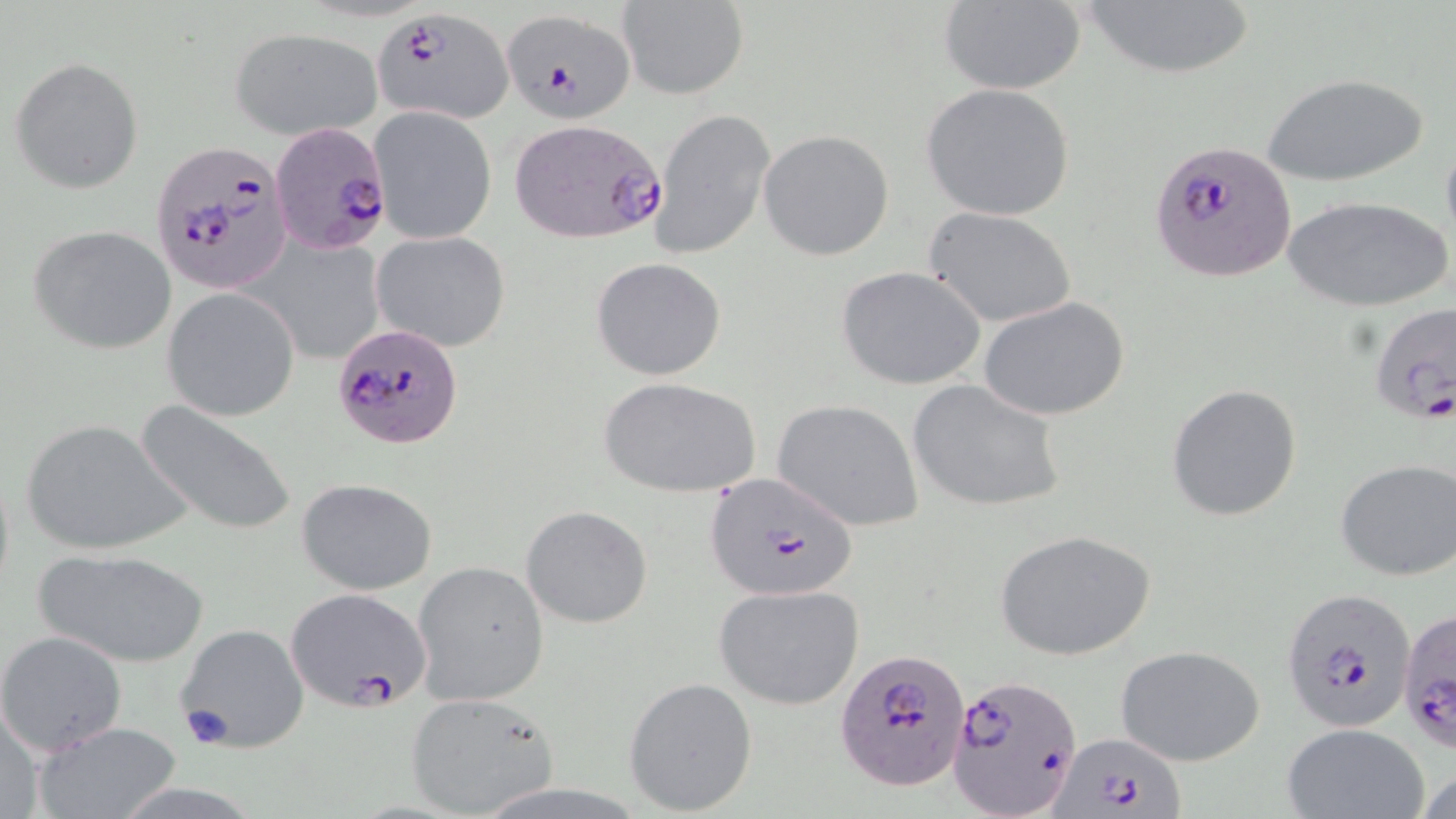

Summary:
  - Coordinate format: approximate bounding boxes as (x1, y1, x2, y2) in pixels
  - Plasmodium falciparum-infected red blood cell locations (subset): (373, 7, 514, 124), (499, 9, 637, 122), (268, 120, 394, 256), (1151, 138, 1297, 283), (151, 140, 291, 296), (1367, 302, 1456, 430), (333, 322, 464, 449), (705, 472, 861, 601), (1283, 586, 1416, 731), (284, 587, 432, 711), (835, 648, 970, 793), (947, 672, 1081, 818), (1049, 733, 1187, 818)
  - Uninfected red blood cell locations (subset): (1083, 0, 1253, 83), (615, 1, 750, 99), (937, 2, 1086, 95), (230, 28, 382, 138), (9, 56, 144, 194), (1260, 70, 1432, 187), (919, 83, 1075, 221), (368, 106, 498, 245), (653, 108, 776, 260), (757, 129, 895, 261), (1284, 197, 1450, 314), (924, 206, 1077, 327), (28, 224, 177, 355), (372, 230, 512, 352), (263, 242, 385, 363), (590, 257, 727, 381), (836, 265, 990, 392), (161, 289, 299, 421), (978, 296, 1130, 421), (600, 378, 760, 498), (905, 378, 1067, 513), (1166, 383, 1302, 523), (771, 398, 925, 531), (135, 401, 301, 537), (19, 419, 187, 555), (1335, 459, 1456, 581), (297, 477, 438, 595), (520, 504, 654, 628), (992, 529, 1157, 662), (33, 548, 209, 670), (413, 561, 550, 706), (713, 583, 864, 711), (174, 622, 311, 754), (0, 630, 128, 754), (1115, 644, 1266, 767), (623, 676, 757, 815), (405, 692, 560, 819), (0, 703, 48, 818), (29, 719, 183, 819), (1281, 723, 1429, 819)
  - Slide-level diagnosis: Plasmodium falciparum
  - Field of view: one of a larger specimen
  - Stain: May-Grünwald-Giemsa
  - Preparation: thin blood film
  - Modality: optical microscopy
  - Image size: 1456×819 pixels
  - Magnification: 1000x